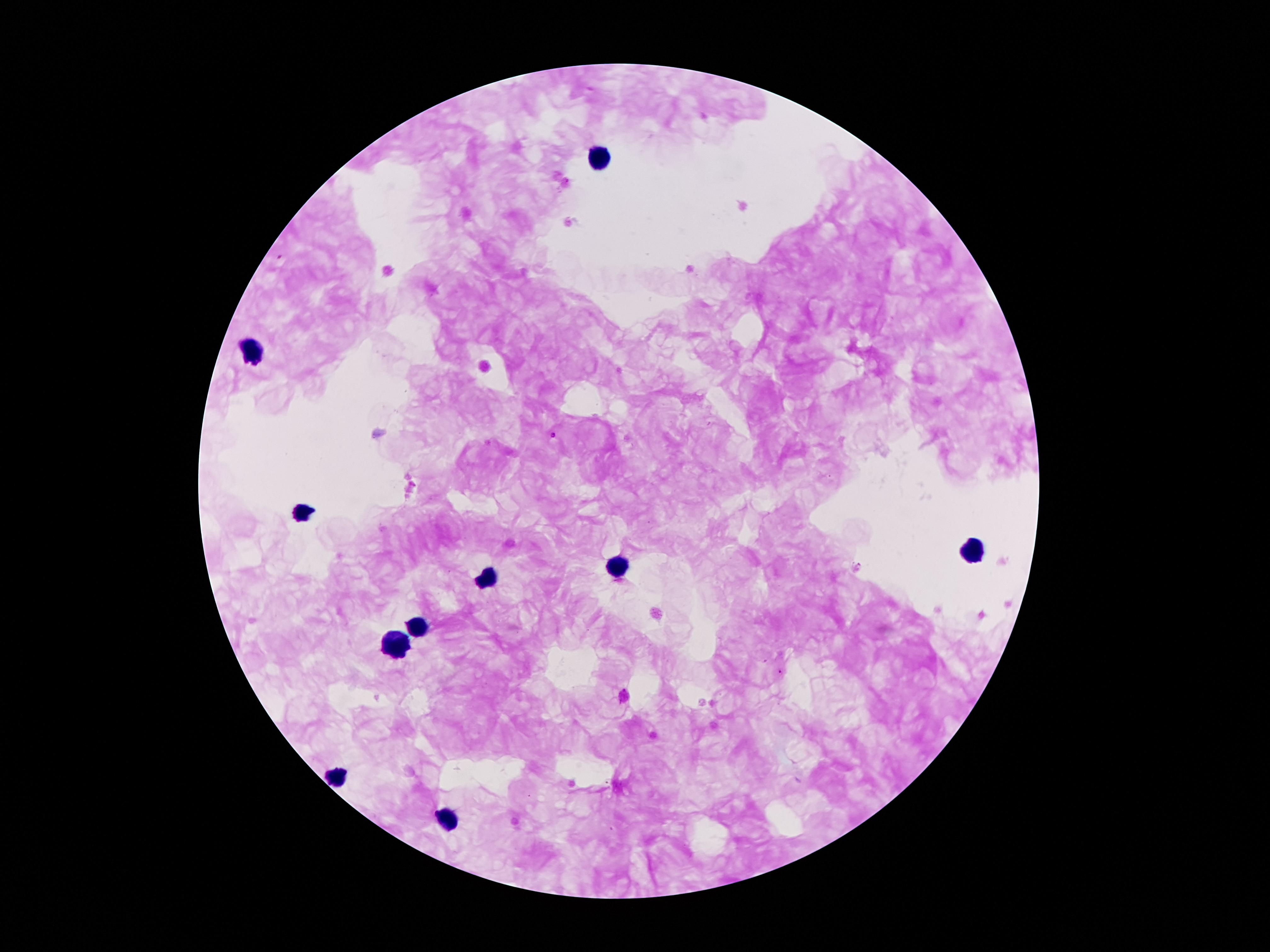

Approximate centers as (x, y) in pixels.
Summary:
  - Leukocyte locations: (599, 155), (251, 353), (303, 513), (971, 550), (618, 567), (486, 575), (414, 628), (395, 646), (339, 777), (444, 816)
  - Plasmodium parasite locations: (553, 435)
  - Field of view: one from this slide
  - Image size: 1270×952 pixels
  - Capture: smartphone through the microscope eyepiece
  - Magnification: 100x
  - Stain: Giemsa
  - Preparation: thick peripheral-blood smear
  - Patient malaria status: positive for Plasmodium falciparum